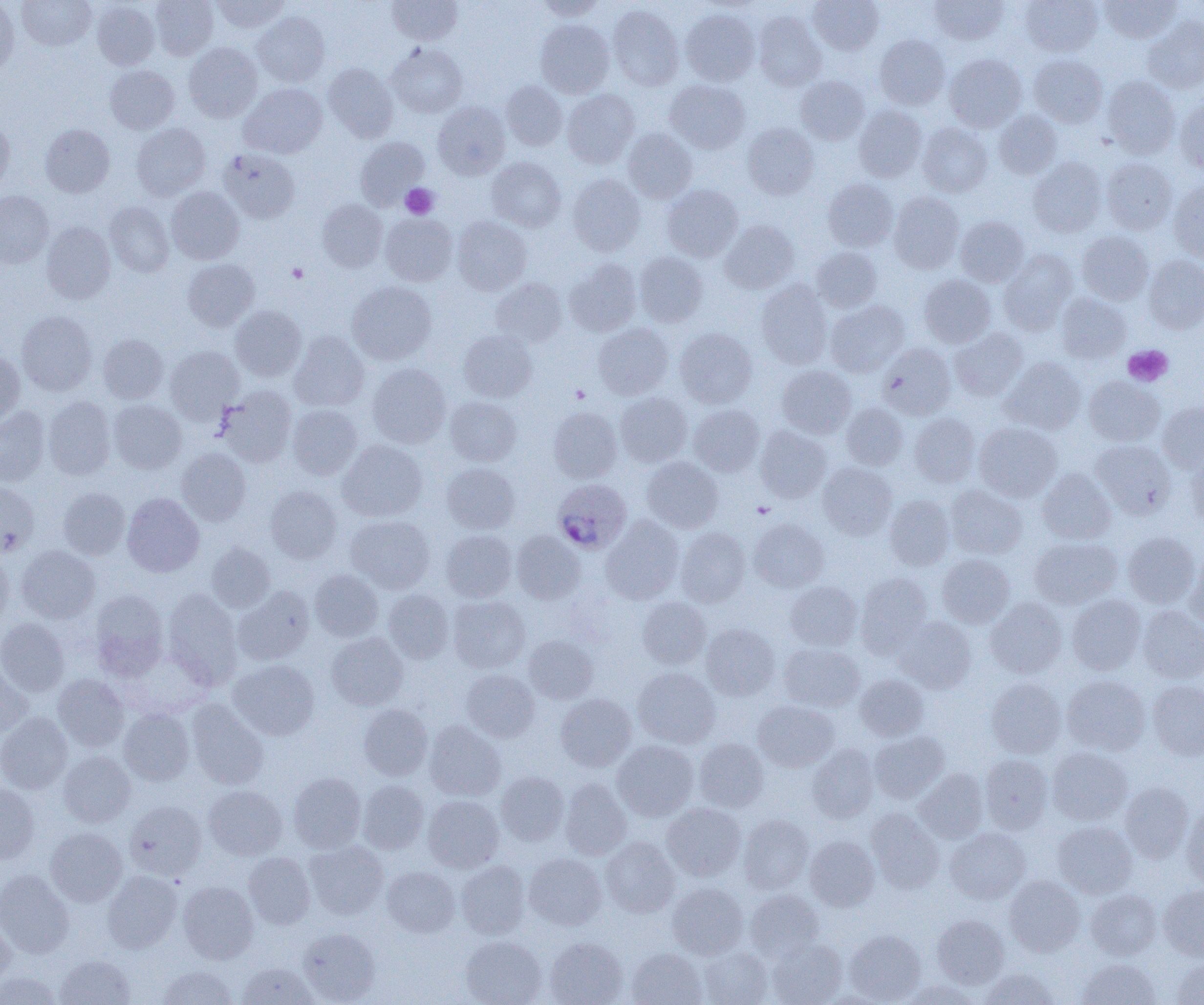

Approximate bounding boxes as named x1/y1/x2/y2 corners in pixels. Platelet locations: (x1=400, y1=183, x2=438, y2=219), (x1=286, y1=263, x2=308, y2=283), (x1=1123, y1=345, x2=1172, y2=386), (x1=570, y1=385, x2=589, y2=402), (x1=753, y1=501, x2=775, y2=518). Plasmodium ovale-infected red blood cell locations: (x1=552, y1=479, x2=632, y2=554). Uninfected red blood cell locations: (x1=0, y1=0, x2=19, y2=79), (x1=17, y1=0, x2=95, y2=50), (x1=149, y1=0, x2=218, y2=60), (x1=210, y1=0, x2=289, y2=33), (x1=387, y1=0, x2=462, y2=45), (x1=535, y1=0, x2=606, y2=20), (x1=808, y1=0, x2=883, y2=54), (x1=929, y1=0, x2=1009, y2=46), (x1=1020, y1=0, x2=1102, y2=56), (x1=1099, y1=0, x2=1181, y2=43), (x1=92, y1=1, x2=159, y2=70), (x1=608, y1=5, x2=684, y2=90), (x1=680, y1=9, x2=760, y2=85), (x1=252, y1=12, x2=330, y2=87), (x1=754, y1=12, x2=826, y2=90), (x1=1142, y1=15, x2=1204, y2=93), (x1=536, y1=20, x2=614, y2=98), (x1=875, y1=34, x2=950, y2=109), (x1=183, y1=43, x2=262, y2=122), (x1=387, y1=43, x2=468, y2=118), (x1=944, y1=53, x2=1027, y2=132), (x1=1028, y1=54, x2=1108, y2=127), (x1=323, y1=63, x2=398, y2=142), (x1=105, y1=65, x2=179, y2=134), (x1=795, y1=75, x2=870, y2=144), (x1=1102, y1=75, x2=1181, y2=159), (x1=665, y1=80, x2=750, y2=153), (x1=501, y1=81, x2=567, y2=150), (x1=239, y1=83, x2=328, y2=158), (x1=562, y1=89, x2=639, y2=169), (x1=1174, y1=100, x2=1204, y2=175), (x1=433, y1=101, x2=510, y2=179), (x1=854, y1=105, x2=927, y2=181), (x1=994, y1=110, x2=1062, y2=179), (x1=0, y1=121, x2=14, y2=193), (x1=131, y1=123, x2=211, y2=201), (x1=743, y1=123, x2=818, y2=199), (x1=917, y1=123, x2=992, y2=197), (x1=40, y1=124, x2=114, y2=197), (x1=623, y1=128, x2=697, y2=203), (x1=355, y1=137, x2=430, y2=208), (x1=218, y1=148, x2=300, y2=223), (x1=1028, y1=156, x2=1106, y2=237), (x1=486, y1=157, x2=566, y2=231), (x1=1102, y1=157, x2=1177, y2=235), (x1=567, y1=174, x2=645, y2=256), (x1=823, y1=179, x2=898, y2=251), (x1=1168, y1=181, x2=1204, y2=261), (x1=662, y1=185, x2=743, y2=261), (x1=166, y1=187, x2=244, y2=264), (x1=0, y1=191, x2=53, y2=267), (x1=889, y1=192, x2=965, y2=274), (x1=317, y1=198, x2=387, y2=272), (x1=105, y1=202, x2=174, y2=277), (x1=380, y1=213, x2=458, y2=286), (x1=452, y1=216, x2=532, y2=294), (x1=955, y1=216, x2=1029, y2=286), (x1=720, y1=220, x2=799, y2=293), (x1=41, y1=221, x2=115, y2=304), (x1=1077, y1=231, x2=1154, y2=305), (x1=811, y1=246, x2=882, y2=312), (x1=998, y1=250, x2=1078, y2=335), (x1=634, y1=252, x2=708, y2=327), (x1=1143, y1=255, x2=1204, y2=334), (x1=182, y1=258, x2=259, y2=331), (x1=564, y1=259, x2=641, y2=336), (x1=919, y1=274, x2=996, y2=348), (x1=491, y1=278, x2=567, y2=347), (x1=756, y1=279, x2=833, y2=369), (x1=346, y1=281, x2=437, y2=364), (x1=1055, y1=292, x2=1131, y2=363), (x1=825, y1=300, x2=910, y2=376), (x1=230, y1=305, x2=306, y2=381), (x1=17, y1=310, x2=97, y2=396), (x1=593, y1=323, x2=674, y2=399), (x1=675, y1=327, x2=757, y2=408), (x1=950, y1=328, x2=1028, y2=400), (x1=458, y1=330, x2=537, y2=402), (x1=289, y1=332, x2=369, y2=411), (x1=98, y1=334, x2=168, y2=403), (x1=878, y1=343, x2=956, y2=419), (x1=165, y1=346, x2=244, y2=422), (x1=0, y1=352, x2=25, y2=425), (x1=1000, y1=357, x2=1086, y2=434), (x1=367, y1=363, x2=451, y2=447), (x1=776, y1=365, x2=856, y2=438), (x1=1083, y1=376, x2=1164, y2=446), (x1=217, y1=386, x2=297, y2=467), (x1=615, y1=391, x2=692, y2=467), (x1=43, y1=396, x2=116, y2=480), (x1=445, y1=396, x2=521, y2=466), (x1=108, y1=399, x2=186, y2=474), (x1=1156, y1=402, x2=1204, y2=473), (x1=841, y1=403, x2=908, y2=470), (x1=286, y1=404, x2=362, y2=479), (x1=688, y1=404, x2=765, y2=476), (x1=0, y1=407, x2=50, y2=487), (x1=548, y1=407, x2=622, y2=483), (x1=910, y1=413, x2=980, y2=487), (x1=974, y1=422, x2=1062, y2=502), (x1=755, y1=425, x2=831, y2=503), (x1=337, y1=440, x2=427, y2=521), (x1=1091, y1=440, x2=1176, y2=519), (x1=176, y1=447, x2=251, y2=526), (x1=1185, y1=450, x2=1204, y2=529), (x1=642, y1=456, x2=723, y2=533), (x1=818, y1=462, x2=897, y2=539), (x1=442, y1=463, x2=520, y2=534), (x1=1037, y1=468, x2=1116, y2=544), (x1=0, y1=481, x2=39, y2=556), (x1=265, y1=485, x2=342, y2=563), (x1=945, y1=485, x2=1027, y2=559), (x1=58, y1=487, x2=130, y2=559), (x1=122, y1=493, x2=204, y2=576), (x1=884, y1=494, x2=955, y2=570), (x1=346, y1=515, x2=435, y2=593), (x1=601, y1=515, x2=683, y2=604), (x1=748, y1=518, x2=829, y2=592), (x1=676, y1=527, x2=750, y2=607), (x1=441, y1=530, x2=516, y2=602), (x1=512, y1=531, x2=585, y2=604), (x1=1123, y1=532, x2=1200, y2=607), (x1=1030, y1=537, x2=1122, y2=609), (x1=206, y1=542, x2=276, y2=613), (x1=16, y1=545, x2=100, y2=624), (x1=0, y1=549, x2=13, y2=628), (x1=937, y1=553, x2=1015, y2=628), (x1=1185, y1=554, x2=1204, y2=629), (x1=310, y1=569, x2=383, y2=641), (x1=856, y1=573, x2=932, y2=655), (x1=785, y1=580, x2=862, y2=650), (x1=233, y1=585, x2=314, y2=665), (x1=89, y1=589, x2=169, y2=680), (x1=163, y1=589, x2=243, y2=688), (x1=383, y1=589, x2=454, y2=663), (x1=1067, y1=594, x2=1146, y2=674), (x1=448, y1=595, x2=530, y2=672), (x1=637, y1=597, x2=711, y2=668), (x1=986, y1=597, x2=1066, y2=678), (x1=1137, y1=605, x2=1204, y2=683), (x1=894, y1=616, x2=976, y2=693), (x1=0, y1=618, x2=69, y2=695), (x1=701, y1=624, x2=780, y2=700), (x1=326, y1=632, x2=408, y2=709), (x1=524, y1=635, x2=598, y2=704), (x1=779, y1=642, x2=865, y2=711), (x1=229, y1=660, x2=319, y2=740), (x1=0, y1=661, x2=32, y2=738), (x1=633, y1=667, x2=720, y2=748), (x1=461, y1=669, x2=540, y2=742), (x1=52, y1=674, x2=129, y2=751), (x1=856, y1=674, x2=930, y2=741), (x1=1062, y1=675, x2=1150, y2=755), (x1=986, y1=678, x2=1066, y2=758), (x1=1148, y1=680, x2=1204, y2=760), (x1=556, y1=693, x2=636, y2=772), (x1=186, y1=699, x2=268, y2=789), (x1=753, y1=700, x2=839, y2=771), (x1=358, y1=704, x2=432, y2=780), (x1=118, y1=708, x2=194, y2=785), (x1=0, y1=711, x2=72, y2=794), (x1=425, y1=720, x2=506, y2=801), (x1=869, y1=731, x2=949, y2=804), (x1=694, y1=738, x2=769, y2=812), (x1=613, y1=740, x2=698, y2=820), (x1=807, y1=744, x2=879, y2=822), (x1=1048, y1=747, x2=1132, y2=825), (x1=59, y1=751, x2=136, y2=826), (x1=979, y1=754, x2=1053, y2=834), (x1=914, y1=768, x2=988, y2=842), (x1=496, y1=771, x2=569, y2=845), (x1=288, y1=772, x2=366, y2=853), (x1=560, y1=778, x2=631, y2=860), (x1=357, y1=779, x2=429, y2=854), (x1=1120, y1=782, x2=1193, y2=862), (x1=0, y1=783, x2=40, y2=865), (x1=204, y1=785, x2=287, y2=859), (x1=423, y1=795, x2=504, y2=872), (x1=124, y1=800, x2=207, y2=881), (x1=661, y1=803, x2=746, y2=881), (x1=1182, y1=803, x2=1204, y2=890), (x1=865, y1=808, x2=944, y2=894), (x1=739, y1=815, x2=814, y2=894), (x1=1053, y1=821, x2=1137, y2=897), (x1=45, y1=827, x2=127, y2=907), (x1=945, y1=828, x2=1030, y2=904), (x1=805, y1=835, x2=879, y2=910), (x1=601, y1=838, x2=680, y2=917), (x1=303, y1=841, x2=388, y2=920), (x1=243, y1=852, x2=315, y2=929), (x1=524, y1=853, x2=607, y2=930), (x1=456, y1=860, x2=530, y2=939), (x1=381, y1=866, x2=460, y2=937), (x1=0, y1=870, x2=75, y2=958), (x1=102, y1=871, x2=182, y2=953), (x1=1004, y1=875, x2=1084, y2=956), (x1=178, y1=881, x2=259, y2=964), (x1=667, y1=882, x2=748, y2=959), (x1=1158, y1=884, x2=1204, y2=960), (x1=1085, y1=889, x2=1161, y2=960), (x1=745, y1=890, x2=824, y2=962), (x1=0, y1=914, x2=16, y2=992), (x1=932, y1=915, x2=1009, y2=988), (x1=297, y1=927, x2=380, y2=1004), (x1=845, y1=929, x2=925, y2=1003), (x1=460, y1=936, x2=547, y2=1005), (x1=545, y1=937, x2=627, y2=1005), (x1=767, y1=938, x2=846, y2=1005), (x1=699, y1=947, x2=773, y2=1005), (x1=626, y1=948, x2=706, y2=1005), (x1=55, y1=955, x2=135, y2=1004), (x1=1078, y1=958, x2=1161, y2=1005), (x1=1170, y1=958, x2=1204, y2=1005), (x1=237, y1=962, x2=318, y2=1005), (x1=157, y1=965, x2=238, y2=1005), (x1=980, y1=968, x2=1061, y2=1004), (x1=0, y1=971, x2=64, y2=1005), (x1=901, y1=980, x2=982, y2=1005). Slide-level diagnosis: Plasmodium ovale. Light microscopy. Thin blood film. Single field of view. Image is 1204×1005 pixels. Captured at 1000x magnification.